Assess this cell for malaria.
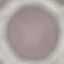
It is uninfected.

Summary:
  - Image type: automatically extracted cell patch, resized to 64 × 64 pixels
  - Preparation: thin blood film
  - Stain: Giemsa
  - Capture: smartphone camera at the microscope eyepiece